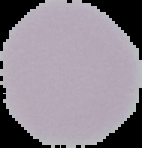

The area outside the segmented cell region is set to black. From a thin blood smear. Malaria status: uninfected. Image is 142×148 pixels.